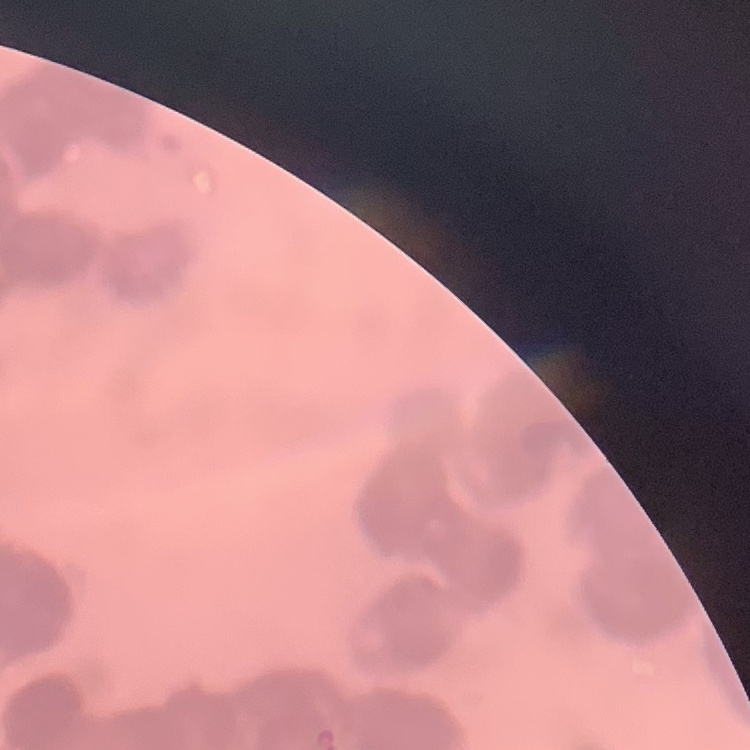
Summary:
  - Erythrocyte morphology: rouleaux formation
  - Stain: Field's or Giemsa
  - Image type: one tile cut from a larger photomicrograph
  - Preparation: thin peripheral smear